Evaluate for malaria.
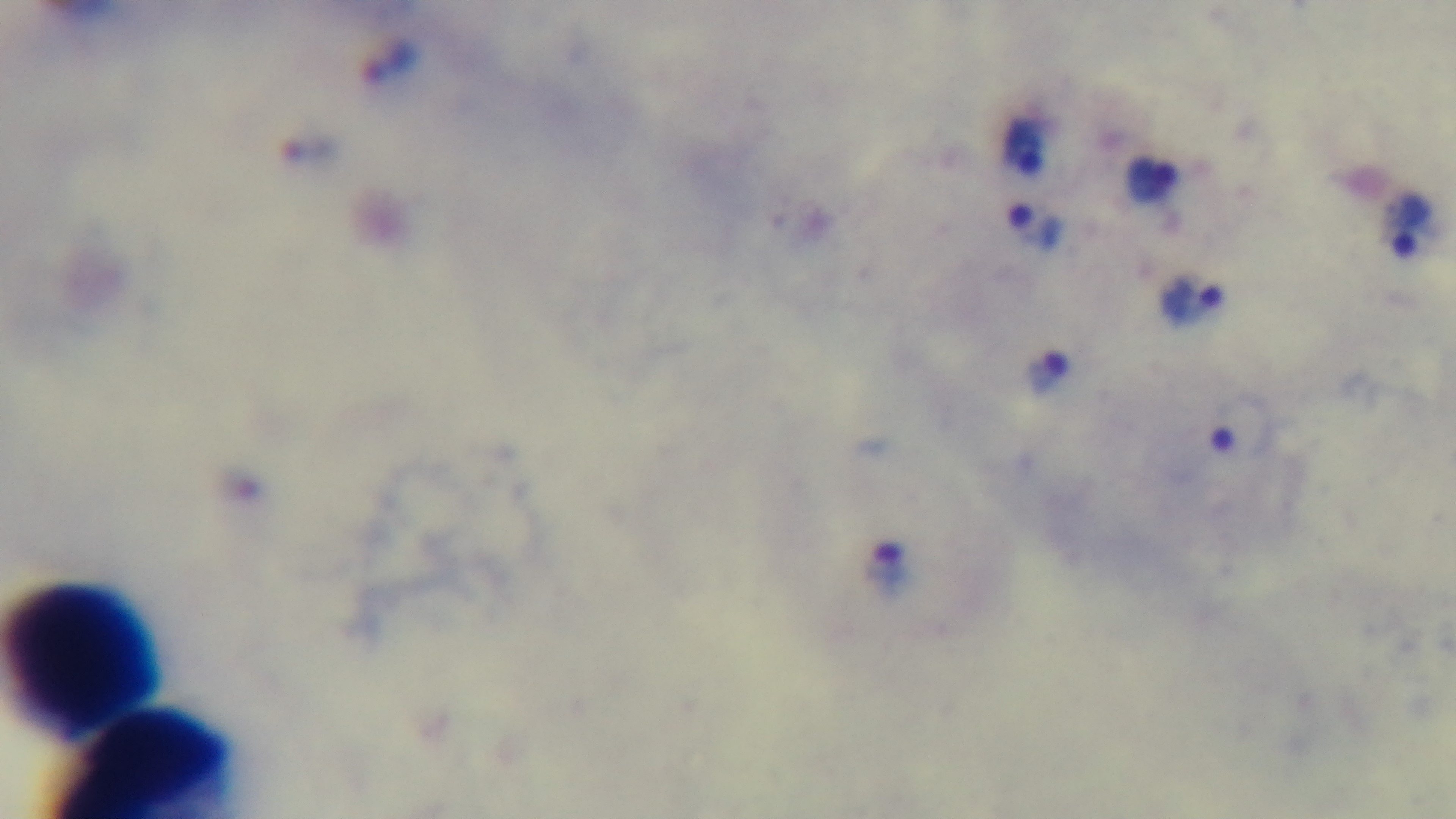

It is infected.

Summary:
  - Stain: Giemsa
  - Capture: mounted 4K digital camera
  - Preparation: thick smear
  - Objective: 100x oil immersion
  - Field of view: single
  - Modality: light microscopy